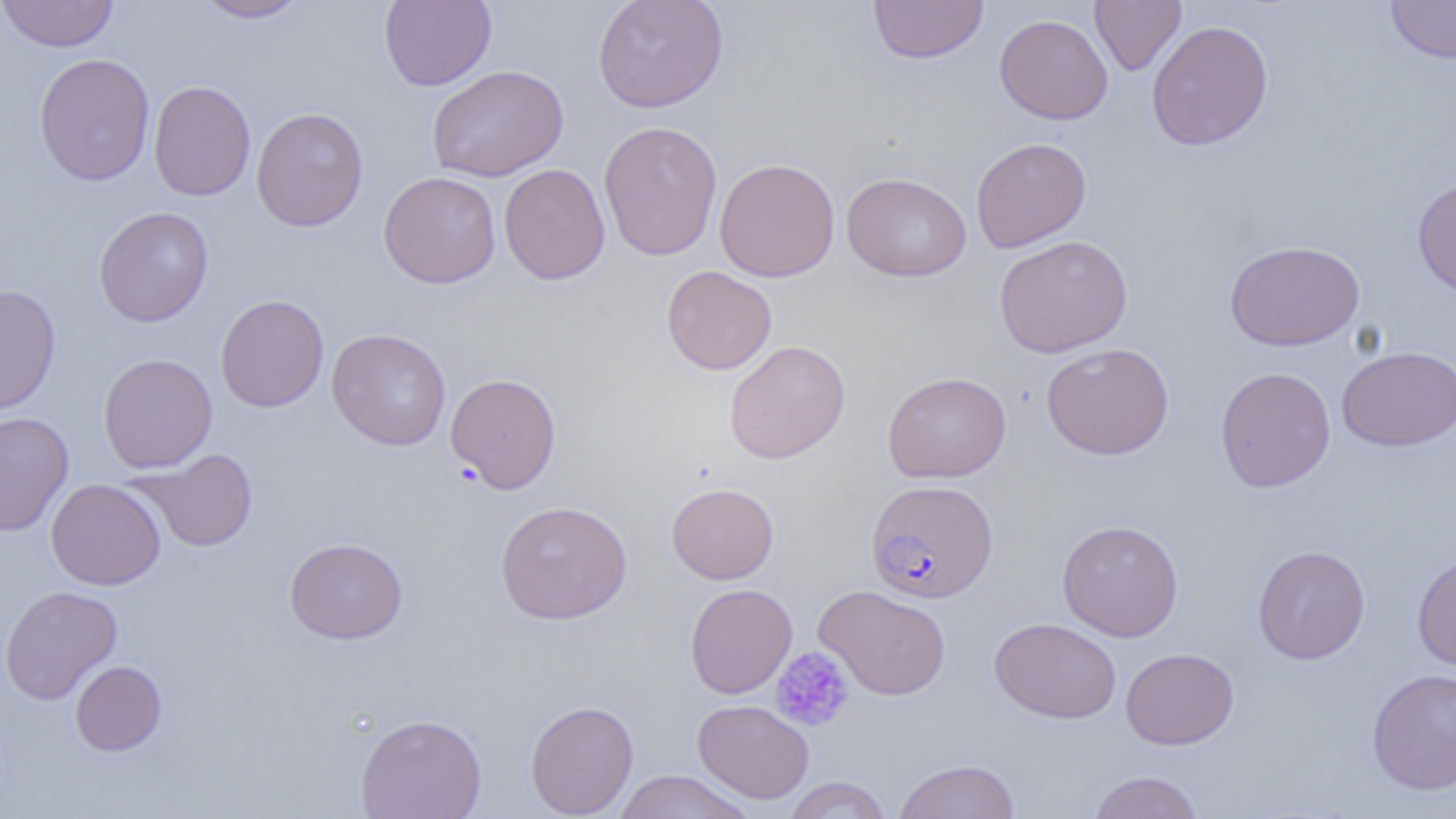
plasmodium_falciparum_infected_red_blood_cell_locations: 'approximate bounding boxes as named x1/y1/x2/y2 corners in pixels: (x1=866, y1=480, x2=998, y2=603)'
slide_level_diagnosis: Plasmodium falciparum
preparation: thin blood film
platelet_locations: 'approximate bounding boxes as named x1/y1/x2/y2 corners in pixels: (x1=770, y1=647, x2=855, y2=733)'
uninfected_red_blood_cell_locations: 'approximate bounding boxes as named x1/y1/x2/y2 corners in pixels: (x1=0, y1=0, x2=120, y2=52), (x1=193, y1=0, x2=311, y2=23), (x1=379, y1=0, x2=497, y2=90), (x1=592, y1=0, x2=728, y2=113), (x1=868, y1=0, x2=988, y2=64), (x1=1089, y1=0, x2=1186, y2=76), (x1=1385, y1=1, x2=1456, y2=63), (x1=994, y1=14, x2=1113, y2=125), (x1=1146, y1=19, x2=1274, y2=150), (x1=33, y1=53, x2=155, y2=186), (x1=427, y1=65, x2=568, y2=182), (x1=148, y1=79, x2=256, y2=201), (x1=250, y1=107, x2=368, y2=231), (x1=598, y1=120, x2=723, y2=260), (x1=971, y1=137, x2=1092, y2=253), (x1=714, y1=158, x2=840, y2=282), (x1=499, y1=163, x2=610, y2=285), (x1=378, y1=171, x2=501, y2=289), (x1=842, y1=172, x2=972, y2=282), (x1=1412, y1=177, x2=1456, y2=297), (x1=94, y1=206, x2=213, y2=327), (x1=994, y1=235, x2=1133, y2=358), (x1=1224, y1=239, x2=1365, y2=351), (x1=661, y1=265, x2=777, y2=375), (x1=0, y1=284, x2=61, y2=415), (x1=215, y1=294, x2=329, y2=412), (x1=327, y1=329, x2=452, y2=451), (x1=723, y1=340, x2=850, y2=464), (x1=1041, y1=342, x2=1175, y2=460), (x1=1336, y1=345, x2=1456, y2=451), (x1=98, y1=353, x2=217, y2=473), (x1=1214, y1=366, x2=1336, y2=492), (x1=882, y1=371, x2=1011, y2=483), (x1=445, y1=372, x2=562, y2=493), (x1=0, y1=412, x2=74, y2=537), (x1=129, y1=448, x2=259, y2=553), (x1=46, y1=478, x2=166, y2=590), (x1=666, y1=482, x2=779, y2=584), (x1=494, y1=500, x2=632, y2=625), (x1=1056, y1=519, x2=1184, y2=642), (x1=284, y1=537, x2=408, y2=645), (x1=1252, y1=545, x2=1370, y2=664), (x1=1412, y1=551, x2=1456, y2=671), (x1=685, y1=583, x2=797, y2=699), (x1=813, y1=584, x2=951, y2=700), (x1=0, y1=585, x2=122, y2=705), (x1=989, y1=617, x2=1121, y2=724), (x1=1120, y1=647, x2=1239, y2=749), (x1=70, y1=660, x2=167, y2=756), (x1=1366, y1=668, x2=1456, y2=795), (x1=525, y1=699, x2=638, y2=818), (x1=692, y1=699, x2=815, y2=804), (x1=355, y1=713, x2=487, y2=819), (x1=892, y1=758, x2=1020, y2=819), (x1=613, y1=770, x2=755, y2=819), (x1=1087, y1=770, x2=1204, y2=818), (x1=783, y1=776, x2=892, y2=818)'
field_of_view: one of a larger specimen
modality: optical microscopy
image_size: 1456×819 pixels
magnification: 1000x